Report the malaria status of this cell.
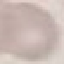

It is uninfected.

stain = Giemsa
image type = automatically extracted cell patch, resized to 64 × 64 pixels
capture = smartphone camera at the microscope eyepiece
preparation = thin blood film